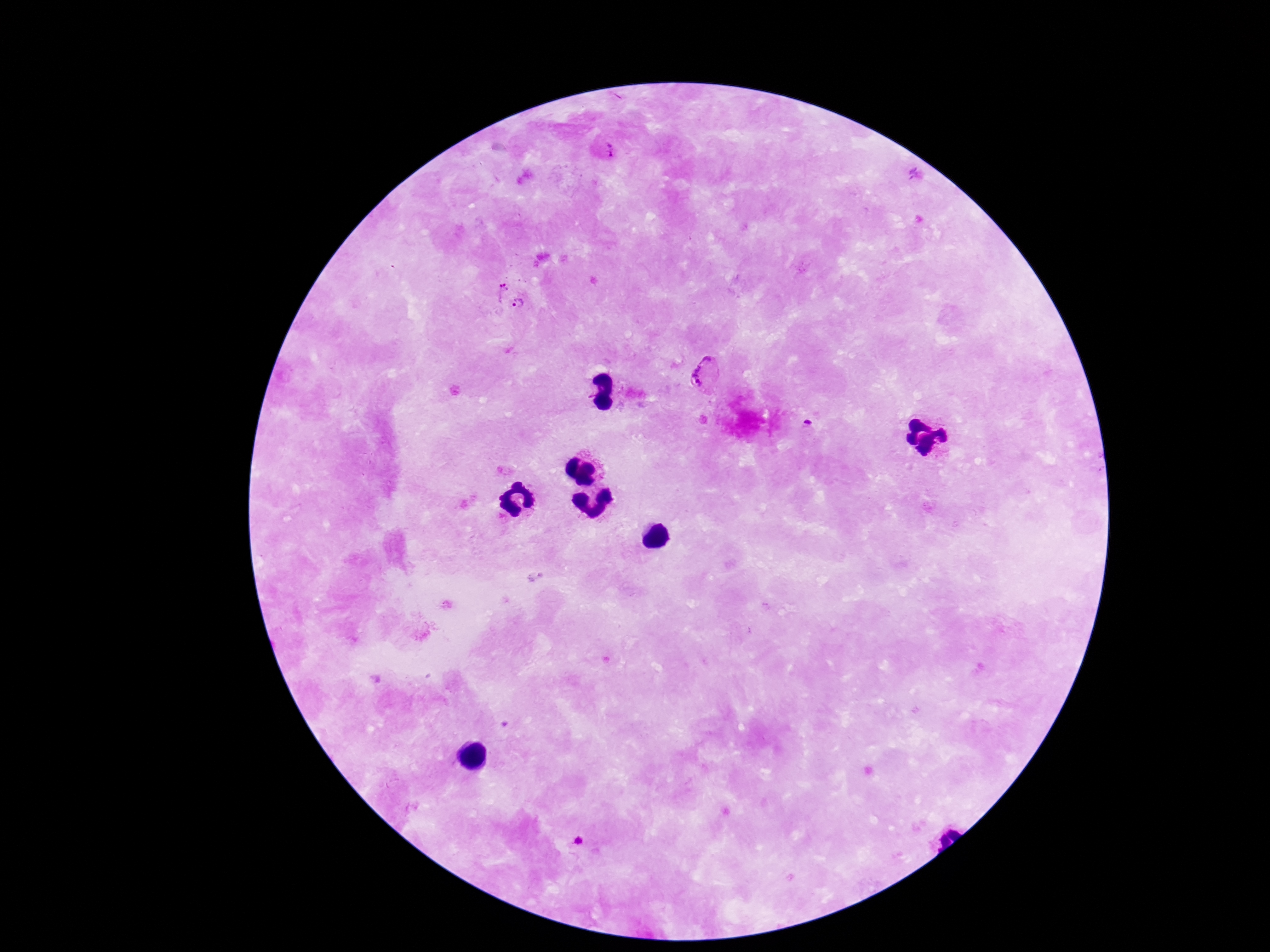
Approximate object centers, in pixels from the top-left corner.
Summary:
  - Plasmodium parasite locations: (x=605, y=153), (x=916, y=176), (x=499, y=281), (x=517, y=306), (x=706, y=375), (x=807, y=426), (x=578, y=840)
  - Preparation: thick blood smear
  - Image size: 1270×952 pixels
  - Patient malaria status: positive
  - Stain: Giemsa
  - Capture: smartphone camera through the microscope eyepiece
  - Field of view: one from this slide
  - Magnification: 100x